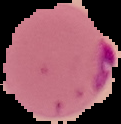
malaria_status: parasitized
image_type: cell region segmented out of the field of view; surrounding area masked to black
image_size: 121×124 pixels
preparation: thin blood film